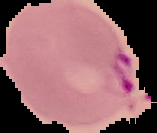
Image is 157×133 pixels. From a thin blood film. Malaria status: parasitized. Segmented cell region on a black background.